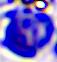

{
  "identification": "leukocyte",
  "modality": "photomicrograph",
  "magnification": "400x"
}